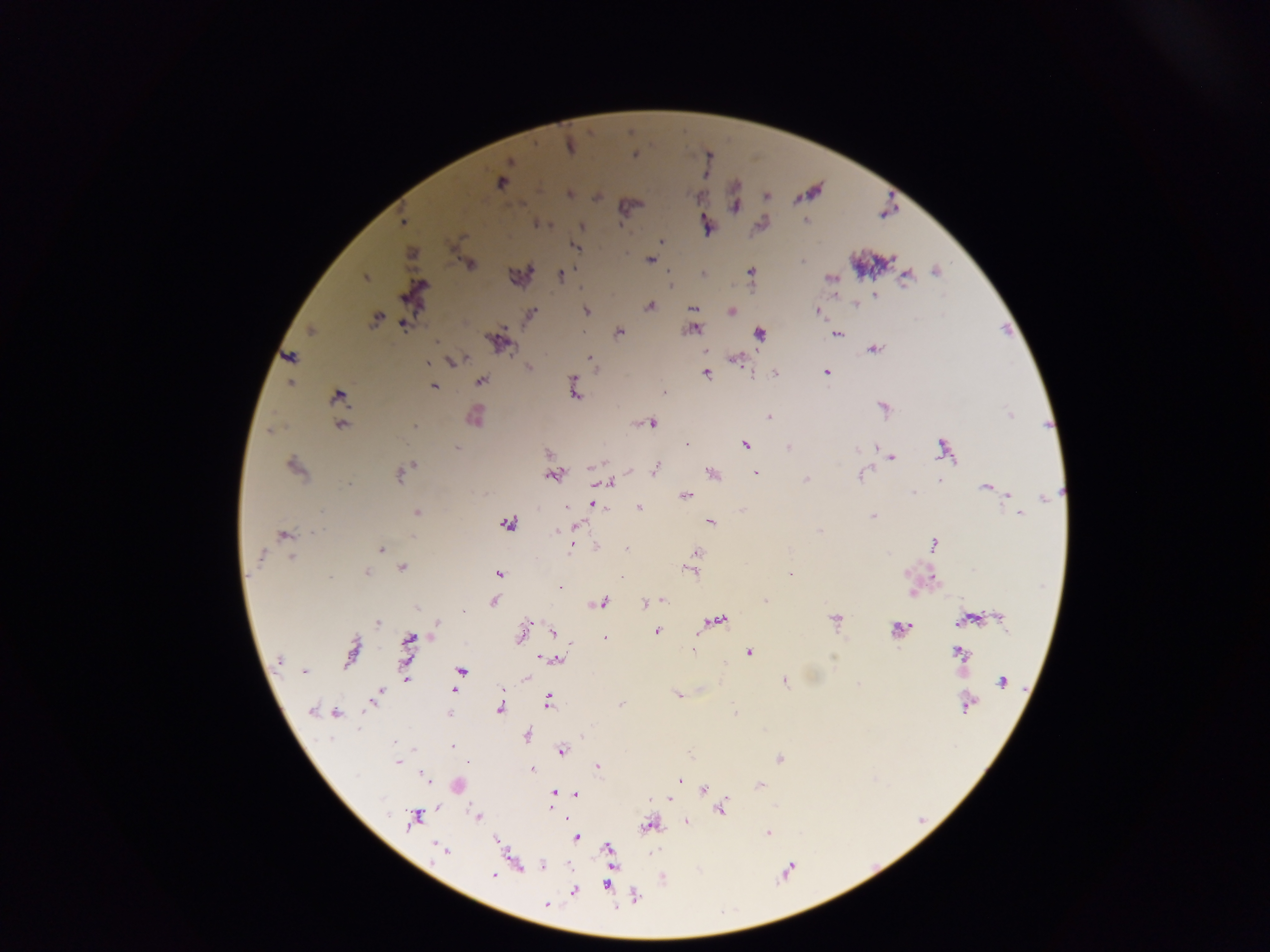
Approximate centers as [x, y] in pixels.
Summary:
  - Malaria parasite locations: [569, 146], [501, 181], [568, 194], [597, 195], [766, 195], [734, 205], [805, 219], [404, 221], [537, 224], [761, 224], [706, 225], [581, 227], [662, 242], [574, 246], [411, 253], [650, 259], [469, 264], [936, 271], [750, 272], [703, 273], [560, 275], [905, 275], [365, 277], [830, 279], [414, 292], [875, 295], [855, 304], [650, 305], [693, 308], [586, 311], [731, 311], [818, 312], [530, 314], [376, 319], [402, 323], [691, 328], [310, 331], [619, 331], [759, 333], [836, 333], [498, 341], [874, 347], [706, 351], [289, 357], [590, 358], [735, 359], [450, 360], [427, 362], [527, 367], [706, 372], [826, 372], [774, 373], [480, 380], [289, 382], [433, 385], [573, 388], [662, 391], [337, 396], [884, 408], [1010, 415], [474, 416], [769, 417], [651, 422], [340, 424], [415, 425], [269, 429], [687, 443], [745, 444], [789, 447], [877, 447], [456, 448], [943, 448], [548, 454], [891, 457], [294, 466], [655, 469], [401, 472], [756, 472], [712, 473], [553, 474], [861, 475], [806, 480], [611, 482], [601, 484], [985, 486], [686, 495], [1044, 495], [1008, 497], [591, 503], [566, 506], [638, 508], [1016, 511], [417, 512], [743, 512], [1020, 514], [873, 516], [709, 521], [506, 524], [574, 527], [820, 530], [283, 534], [933, 544], [596, 546], [571, 547], [381, 549], [626, 549], [696, 553], [261, 555], [291, 557], [401, 568], [691, 571], [366, 573], [790, 573], [497, 574], [559, 587], [911, 593], [661, 600], [764, 600], [494, 601], [651, 601], [599, 603], [646, 604], [417, 607], [997, 616], [836, 618], [964, 619], [716, 621], [377, 622], [438, 624], [898, 629], [553, 631], [656, 631], [522, 633], [606, 639], [407, 643], [569, 643], [692, 649], [352, 650], [959, 651], [749, 652], [541, 656], [555, 658], [278, 660], [461, 670], [304, 672], [526, 677], [407, 678], [783, 680], [1002, 682], [455, 689], [677, 693], [374, 697], [547, 700], [966, 703], [499, 708], [312, 710], [323, 712], [335, 712], [448, 713], [735, 713], [526, 735], [451, 746], [561, 750], [779, 759], [398, 762], [598, 765], [532, 768], [423, 775], [679, 780], [457, 785], [759, 786], [703, 790], [554, 792], [576, 794], [669, 799], [721, 808], [477, 816], [413, 818], [686, 821], [648, 825], [767, 833], [575, 837], [497, 841], [608, 848], [443, 850], [542, 865], [518, 866], [494, 875], [607, 885], [574, 890], [634, 895], [546, 904]
  - Capture: mobile-phone photograph through a microscope
  - Field of view: single
  - Preparation: thick blood film
  - Country: Ghana
  - Image size: 1270×952 pixels